Describe the morphology of the red blood cells.
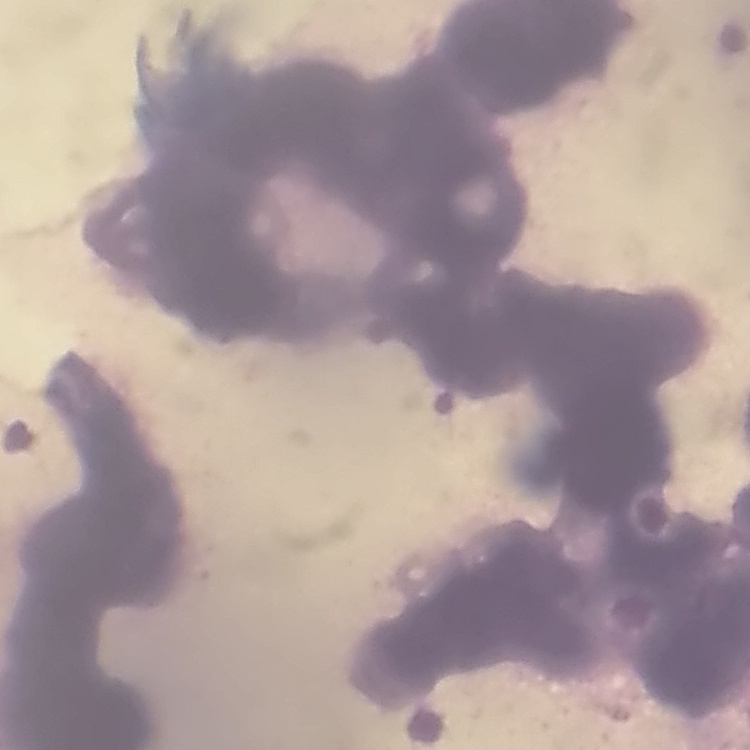
Rouleaux formation.

Stained with either Field's or Giemsa. Thin peripheral smear. One tile cut from a larger photomicrograph.